Give the extent of all Plasmodium ovale-infected red blood cells.
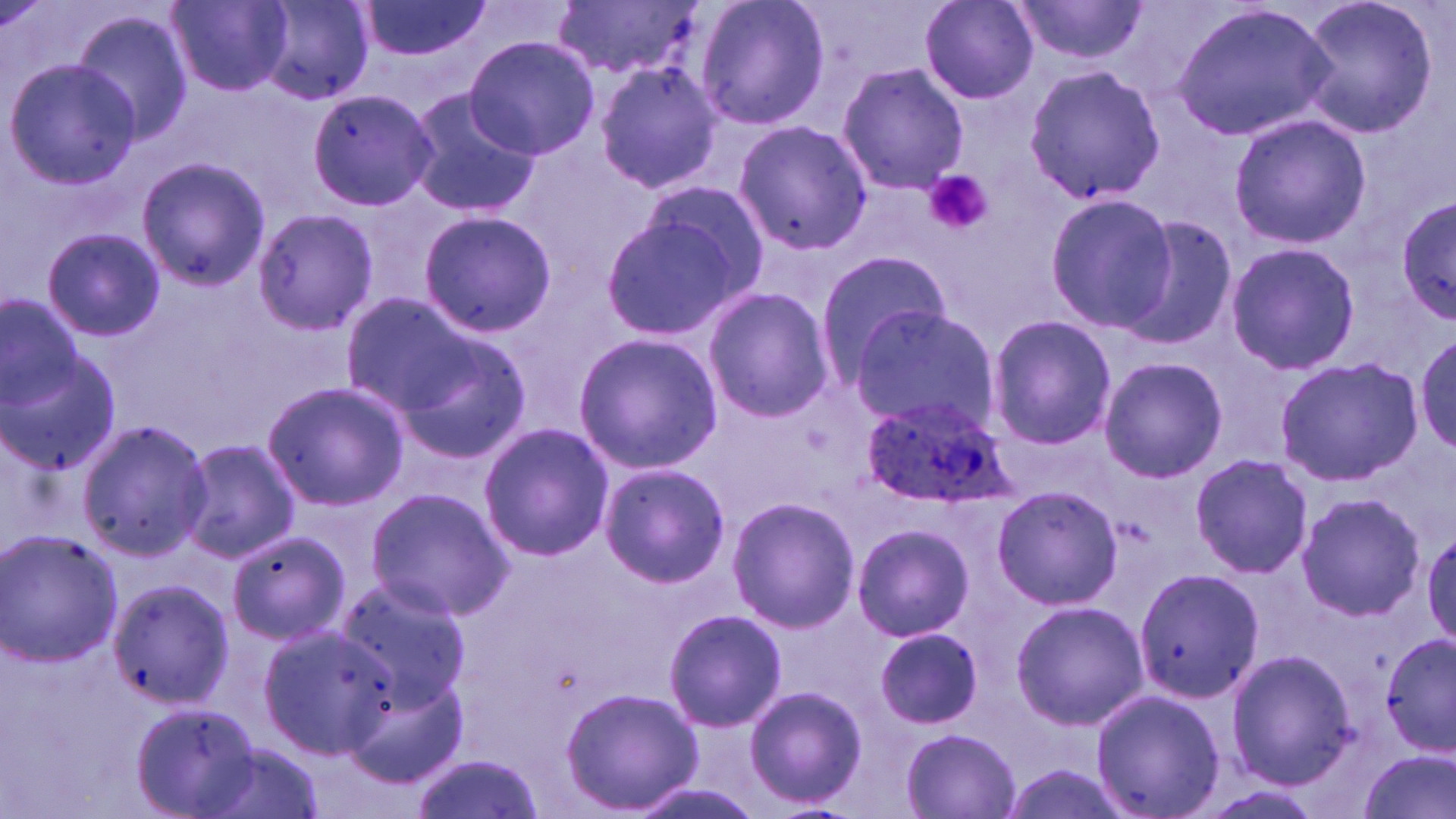

Approximate bounding boxes as named x1/y1/x2/y2 corners in pixels.
Plasmodium ovale-infected red blood cells: (x1=859, y1=396, x2=1016, y2=510).

slide-level diagnosis = Plasmodium ovale
uninfected red blood cell locations = approximate bounding boxes as named x1/y1/x2/y2 corners in pixels: (x1=169, y1=0, x2=291, y2=95), (x1=358, y1=0, x2=489, y2=61), (x1=560, y1=0, x2=702, y2=80), (x1=694, y1=0, x2=831, y2=131), (x1=919, y1=0, x2=1040, y2=104), (x1=1010, y1=0, x2=1149, y2=64), (x1=1296, y1=0, x2=1441, y2=142), (x1=255, y1=2, x2=375, y2=106), (x1=1170, y1=4, x2=1339, y2=141), (x1=70, y1=16, x2=192, y2=146), (x1=464, y1=36, x2=598, y2=161), (x1=4, y1=60, x2=142, y2=190), (x1=593, y1=60, x2=724, y2=194), (x1=1021, y1=62, x2=1169, y2=206), (x1=836, y1=63, x2=969, y2=194), (x1=304, y1=88, x2=435, y2=209), (x1=400, y1=89, x2=538, y2=219), (x1=1228, y1=112, x2=1373, y2=248), (x1=732, y1=120, x2=873, y2=254), (x1=136, y1=157, x2=271, y2=290), (x1=631, y1=178, x2=772, y2=306), (x1=1043, y1=192, x2=1176, y2=333), (x1=1396, y1=197, x2=1456, y2=317), (x1=252, y1=207, x2=377, y2=336), (x1=597, y1=207, x2=753, y2=345), (x1=419, y1=211, x2=556, y2=336), (x1=1117, y1=211, x2=1240, y2=351), (x1=42, y1=227, x2=165, y2=343), (x1=1223, y1=241, x2=1359, y2=377), (x1=815, y1=251, x2=953, y2=382), (x1=702, y1=285, x2=835, y2=424), (x1=0, y1=294, x2=84, y2=428), (x1=355, y1=297, x2=530, y2=453), (x1=845, y1=307, x2=1000, y2=434), (x1=985, y1=314, x2=1117, y2=450), (x1=1, y1=328, x2=122, y2=478), (x1=1413, y1=329, x2=1456, y2=456), (x1=571, y1=332, x2=724, y2=472), (x1=1097, y1=355, x2=1229, y2=483), (x1=1275, y1=355, x2=1423, y2=486), (x1=263, y1=381, x2=410, y2=510), (x1=76, y1=418, x2=211, y2=561), (x1=478, y1=421, x2=613, y2=561), (x1=181, y1=438, x2=300, y2=563), (x1=1189, y1=454, x2=1314, y2=578), (x1=598, y1=464, x2=731, y2=586), (x1=992, y1=485, x2=1123, y2=610), (x1=366, y1=487, x2=515, y2=619), (x1=1295, y1=492, x2=1425, y2=621), (x1=727, y1=496, x2=859, y2=633), (x1=852, y1=522, x2=975, y2=643), (x1=0, y1=528, x2=122, y2=667), (x1=226, y1=529, x2=351, y2=643), (x1=1130, y1=568, x2=1264, y2=705), (x1=330, y1=575, x2=473, y2=710), (x1=105, y1=578, x2=233, y2=708), (x1=1010, y1=598, x2=1147, y2=732), (x1=663, y1=608, x2=789, y2=733), (x1=256, y1=624, x2=397, y2=756), (x1=873, y1=627, x2=984, y2=729), (x1=1378, y1=634, x2=1456, y2=754), (x1=1225, y1=646, x2=1358, y2=791), (x1=344, y1=671, x2=469, y2=787), (x1=742, y1=684, x2=868, y2=810), (x1=559, y1=686, x2=703, y2=813), (x1=1089, y1=687, x2=1226, y2=819), (x1=132, y1=701, x2=260, y2=817), (x1=899, y1=728, x2=1022, y2=817), (x1=198, y1=742, x2=326, y2=819), (x1=1355, y1=752, x2=1455, y2=819), (x1=415, y1=754, x2=539, y2=818)
stain = May-Grünwald-Giemsa
magnification = 1000x
preparation = thin blood film
image size = 1456×819 pixels
platelet locations = approximate bounding boxes as named x1/y1/x2/y2 corners in pixels: (x1=923, y1=171, x2=993, y2=236)
field of view = single
modality = light microscopy